Report the malaria status of this cell.
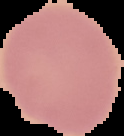
Uninfected.

Image is 124×136 pixels. From a thin blood smear. Segmented cell region on a black background.